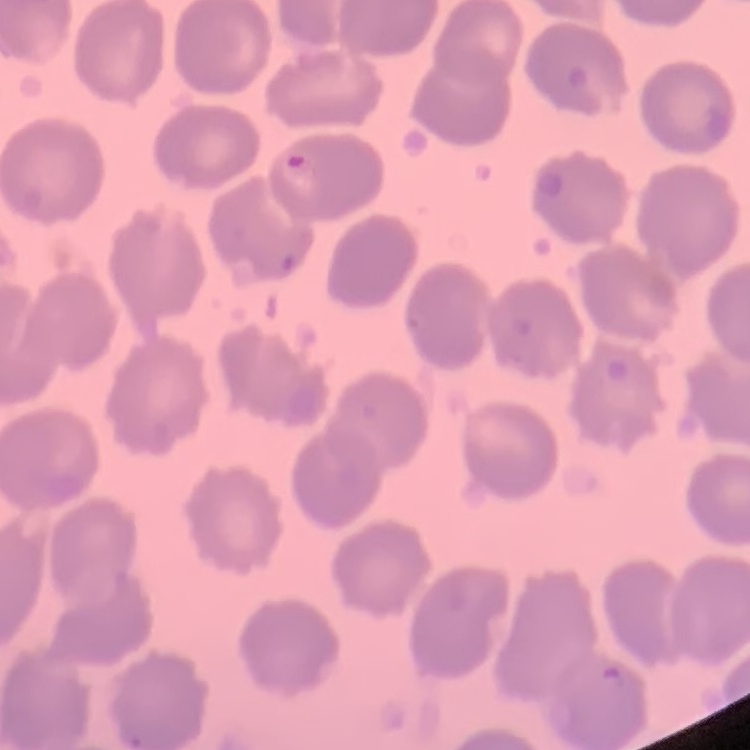

The erythrocytes show no rouleaux formation. Field's or Giemsa stain. Square crop of a larger photomicrograph. Thin blood smear.